Identify the parasite.
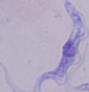
This is a trypanosome.

Micrograph. Captured at 1000x magnification.